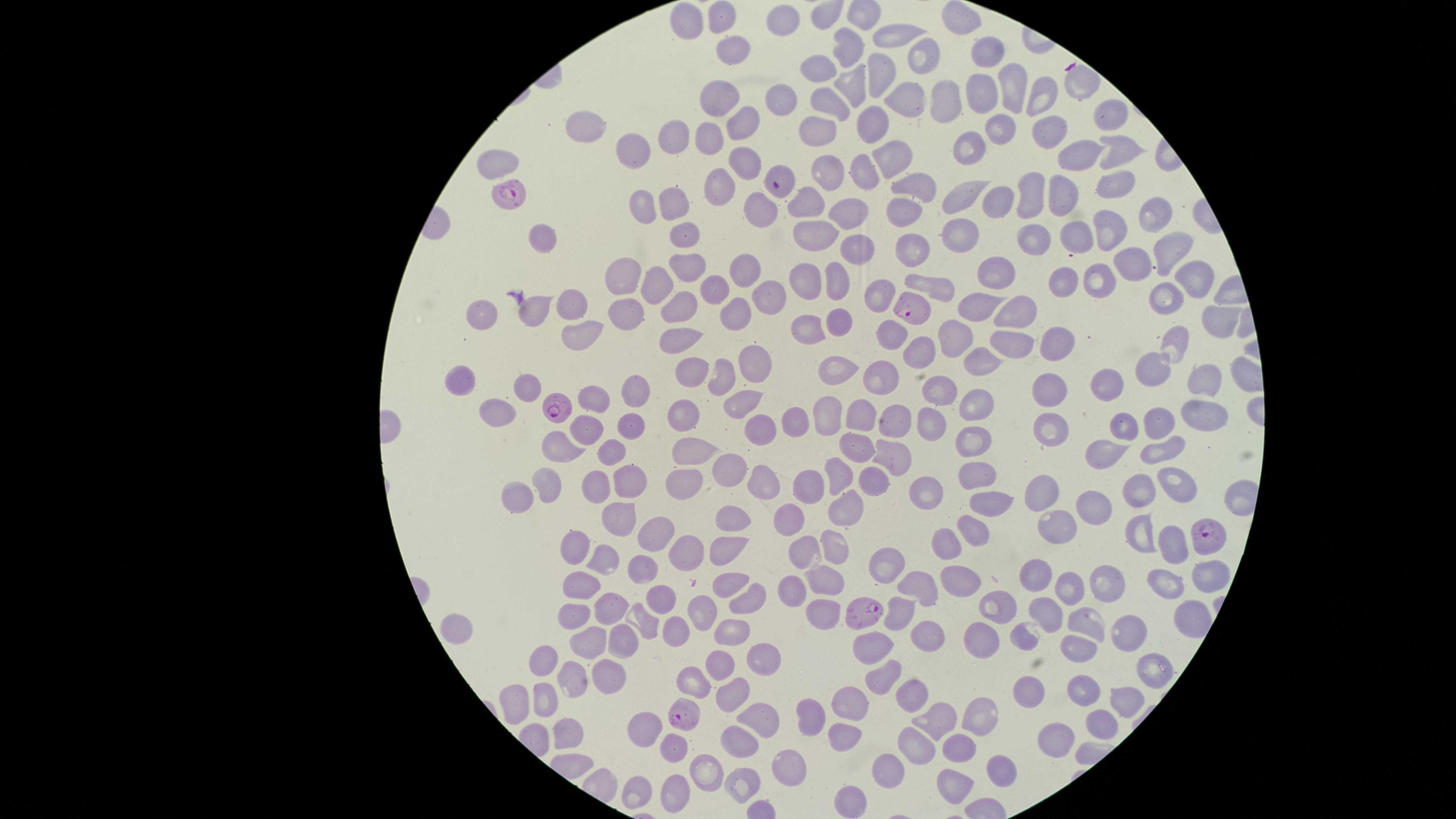

Approximate marker points, in pixels from the top-left corner. Parasitized red blood cells: (x=779, y=182), (x=514, y=191), (x=910, y=310), (x=555, y=405), (x=1208, y=537), (x=863, y=609), (x=686, y=715). Uninfected red blood cells: (x=721, y=15), (x=691, y=17), (x=785, y=18), (x=959, y=26), (x=894, y=35), (x=849, y=51), (x=730, y=53), (x=990, y=55), (x=916, y=58), (x=821, y=69), (x=882, y=71), (x=856, y=82), (x=1010, y=89), (x=1044, y=91), (x=983, y=96), (x=721, y=97), (x=949, y=99), (x=829, y=100), (x=904, y=100), (x=772, y=103), (x=1102, y=114), (x=741, y=125), (x=870, y=125), (x=1000, y=127), (x=582, y=129), (x=814, y=129), (x=1044, y=130), (x=674, y=137), (x=707, y=140), (x=633, y=147), (x=1120, y=147), (x=897, y=151), (x=968, y=151), (x=1081, y=155), (x=502, y=161), (x=741, y=161), (x=862, y=169), (x=826, y=171), (x=1113, y=177), (x=724, y=184), (x=915, y=185), (x=969, y=194), (x=1066, y=197), (x=1032, y=198), (x=811, y=202), (x=678, y=203), (x=644, y=204), (x=1001, y=204), (x=761, y=207), (x=903, y=210), (x=854, y=212), (x=1152, y=213), (x=1111, y=229), (x=683, y=231), (x=810, y=233), (x=958, y=233), (x=1072, y=236), (x=539, y=237), (x=1035, y=240), (x=909, y=244), (x=850, y=245), (x=1172, y=248), (x=684, y=264), (x=1130, y=267), (x=746, y=269), (x=1001, y=270), (x=810, y=272), (x=1192, y=277), (x=1101, y=279), (x=659, y=280), (x=841, y=280), (x=629, y=281), (x=1056, y=284), (x=941, y=287), (x=713, y=288), (x=877, y=291), (x=772, y=296), (x=1165, y=298), (x=979, y=304), (x=573, y=305), (x=1010, y=305), (x=680, y=306), (x=629, y=308), (x=739, y=311), (x=487, y=313), (x=532, y=313), (x=1222, y=316), (x=834, y=322), (x=806, y=331), (x=575, y=332), (x=892, y=334), (x=959, y=336), (x=1056, y=337), (x=1180, y=341), (x=674, y=342), (x=1001, y=344), (x=920, y=349), (x=978, y=359), (x=749, y=361), (x=1149, y=365), (x=837, y=367), (x=691, y=368), (x=720, y=370), (x=879, y=375), (x=1207, y=378), (x=463, y=379), (x=1052, y=386), (x=1109, y=386), (x=524, y=390), (x=640, y=390), (x=594, y=394), (x=948, y=394), (x=983, y=398), (x=740, y=403), (x=498, y=414), (x=826, y=414), (x=857, y=414), (x=1206, y=414), (x=684, y=415), (x=1158, y=418), (x=935, y=421), (x=798, y=422), (x=1124, y=423), (x=631, y=425), (x=899, y=425), (x=587, y=429), (x=757, y=429), (x=1058, y=430), (x=969, y=438), (x=561, y=445), (x=1156, y=445), (x=1109, y=447), (x=854, y=449), (x=611, y=451), (x=696, y=454), (x=890, y=460), (x=736, y=473), (x=834, y=474), (x=975, y=474), (x=870, y=480), (x=1177, y=480), (x=764, y=482), (x=628, y=483), (x=681, y=487), (x=809, y=487), (x=1040, y=489), (x=550, y=491), (x=594, y=491), (x=1140, y=493), (x=924, y=495), (x=517, y=496), (x=989, y=503), (x=1084, y=507), (x=843, y=512), (x=729, y=516), (x=617, y=518), (x=790, y=519), (x=1061, y=526), (x=663, y=531), (x=973, y=533), (x=1139, y=535), (x=947, y=541), (x=725, y=543), (x=1169, y=543), (x=831, y=545), (x=689, y=547), (x=804, y=549), (x=576, y=552), (x=600, y=560), (x=644, y=563), (x=888, y=568), (x=1032, y=572), (x=826, y=574), (x=955, y=575), (x=1209, y=575), (x=730, y=579), (x=1105, y=580), (x=1064, y=584), (x=1169, y=584), (x=579, y=585), (x=923, y=586), (x=794, y=588), (x=665, y=596), (x=747, y=603), (x=824, y=607), (x=612, y=608), (x=997, y=611), (x=899, y=613), (x=709, y=614), (x=1046, y=614), (x=578, y=618), (x=643, y=618), (x=1086, y=620), (x=1189, y=620), (x=676, y=629), (x=731, y=630), (x=927, y=630), (x=459, y=632), (x=1025, y=635), (x=1126, y=635), (x=981, y=636), (x=618, y=640), (x=585, y=642), (x=876, y=644), (x=1070, y=652), (x=762, y=653), (x=543, y=661), (x=718, y=661), (x=1151, y=668), (x=885, y=669), (x=693, y=676), (x=610, y=680), (x=574, y=682), (x=1081, y=682), (x=731, y=689), (x=907, y=689), (x=507, y=700), (x=1121, y=701), (x=542, y=702), (x=846, y=704), (x=768, y=711), (x=986, y=715), (x=809, y=718), (x=939, y=718), (x=645, y=722), (x=1097, y=726), (x=844, y=734), (x=567, y=736), (x=1056, y=737), (x=742, y=738), (x=672, y=742), (x=961, y=745), (x=912, y=749), (x=786, y=759), (x=703, y=764), (x=999, y=772), (x=885, y=776), (x=739, y=777), (x=953, y=785), (x=635, y=793), (x=671, y=795), (x=848, y=798). Species: Plasmodium falciparum. Circular visible region. Thin blood smear. Smartphone photograph through the microscope eyepiece. One field of view of the specimen. Presence: malaria parasites seen. Image is 1456×819 pixels. Giemsa-stained preparation.